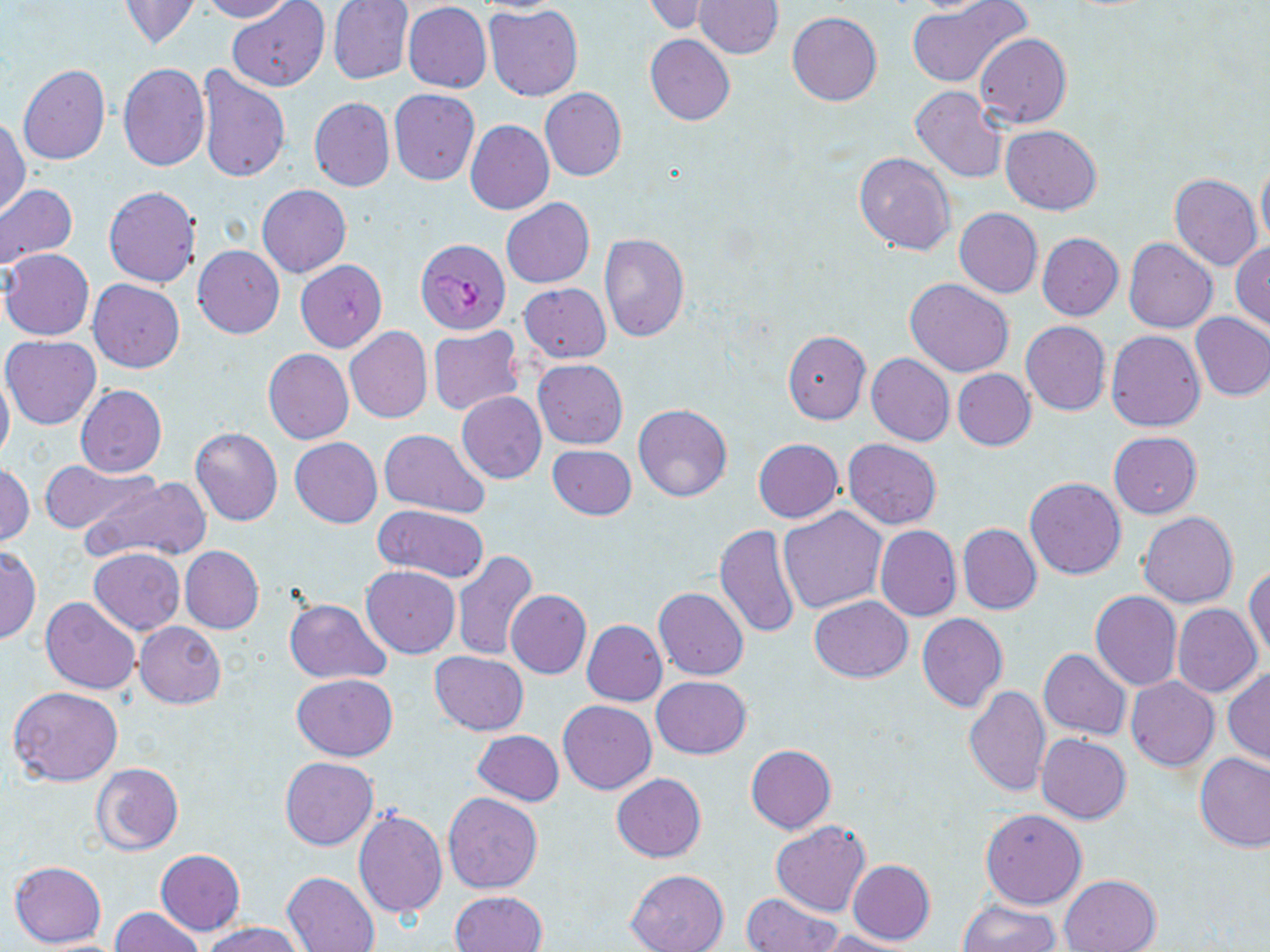
Approximate bounding boxes as named x1/y1/x2/y2 corners in pixels. Plasmodium falciparum-infected red blood cell locations: (x1=416, y1=238, x2=511, y2=334). Uninfected red blood cell locations: (x1=199, y1=0, x2=296, y2=22), (x1=641, y1=0, x2=720, y2=35), (x1=695, y1=0, x2=783, y2=58), (x1=903, y1=0, x2=1009, y2=16), (x1=119, y1=1, x2=201, y2=50), (x1=228, y1=1, x2=330, y2=91), (x1=327, y1=2, x2=414, y2=86), (x1=403, y1=2, x2=492, y2=93), (x1=907, y1=3, x2=1030, y2=88), (x1=484, y1=5, x2=583, y2=101), (x1=787, y1=11, x2=882, y2=105), (x1=975, y1=33, x2=1070, y2=127), (x1=645, y1=34, x2=735, y2=125), (x1=118, y1=63, x2=209, y2=172), (x1=18, y1=64, x2=110, y2=164), (x1=197, y1=64, x2=290, y2=183), (x1=910, y1=86, x2=1008, y2=183), (x1=541, y1=87, x2=626, y2=181), (x1=389, y1=89, x2=479, y2=186), (x1=310, y1=98, x2=395, y2=192), (x1=0, y1=117, x2=30, y2=217), (x1=877, y1=119, x2=985, y2=238), (x1=467, y1=121, x2=554, y2=215), (x1=1000, y1=125, x2=1102, y2=215), (x1=854, y1=151, x2=956, y2=256), (x1=1256, y1=162, x2=1270, y2=252), (x1=1169, y1=173, x2=1262, y2=271), (x1=0, y1=182, x2=77, y2=270), (x1=103, y1=185, x2=201, y2=287), (x1=257, y1=185, x2=351, y2=278), (x1=501, y1=198, x2=594, y2=288), (x1=954, y1=208, x2=1042, y2=297), (x1=598, y1=233, x2=689, y2=342), (x1=1036, y1=233, x2=1124, y2=321), (x1=1124, y1=238, x2=1217, y2=333), (x1=1230, y1=242, x2=1270, y2=332), (x1=193, y1=245, x2=284, y2=338), (x1=1, y1=249, x2=94, y2=341), (x1=295, y1=260, x2=388, y2=352), (x1=88, y1=278, x2=184, y2=373), (x1=905, y1=279, x2=1015, y2=377), (x1=520, y1=282, x2=611, y2=363), (x1=1190, y1=312, x2=1270, y2=402), (x1=1021, y1=320, x2=1110, y2=415), (x1=345, y1=326, x2=432, y2=423), (x1=428, y1=326, x2=523, y2=416), (x1=1105, y1=330, x2=1205, y2=431), (x1=782, y1=331, x2=871, y2=423), (x1=1, y1=335, x2=101, y2=429), (x1=263, y1=348, x2=353, y2=444), (x1=866, y1=353, x2=954, y2=447), (x1=534, y1=359, x2=628, y2=449), (x1=953, y1=369, x2=1035, y2=450), (x1=0, y1=370, x2=14, y2=466), (x1=76, y1=385, x2=167, y2=478), (x1=457, y1=392, x2=547, y2=483), (x1=633, y1=404, x2=733, y2=502), (x1=190, y1=427, x2=282, y2=526), (x1=379, y1=429, x2=490, y2=516), (x1=1109, y1=432, x2=1202, y2=518), (x1=291, y1=438, x2=381, y2=527), (x1=753, y1=439, x2=842, y2=523), (x1=843, y1=439, x2=941, y2=529), (x1=547, y1=444, x2=636, y2=520), (x1=42, y1=460, x2=156, y2=536), (x1=1, y1=464, x2=33, y2=547), (x1=81, y1=475, x2=212, y2=565), (x1=1025, y1=477, x2=1126, y2=579), (x1=373, y1=505, x2=488, y2=583), (x1=778, y1=507, x2=887, y2=614), (x1=1139, y1=511, x2=1238, y2=607), (x1=714, y1=523, x2=801, y2=639), (x1=957, y1=524, x2=1041, y2=615), (x1=875, y1=525, x2=962, y2=622), (x1=0, y1=546, x2=41, y2=643), (x1=180, y1=546, x2=264, y2=634), (x1=89, y1=548, x2=185, y2=634), (x1=451, y1=550, x2=539, y2=661), (x1=1246, y1=563, x2=1269, y2=663), (x1=361, y1=566, x2=460, y2=658), (x1=653, y1=586, x2=749, y2=681), (x1=505, y1=589, x2=591, y2=679), (x1=1090, y1=591, x2=1181, y2=690), (x1=809, y1=595, x2=913, y2=682), (x1=40, y1=597, x2=140, y2=695), (x1=283, y1=598, x2=391, y2=684), (x1=1173, y1=604, x2=1261, y2=697), (x1=917, y1=613, x2=1008, y2=712), (x1=581, y1=620, x2=666, y2=706), (x1=134, y1=621, x2=225, y2=708), (x1=1038, y1=649, x2=1131, y2=740), (x1=431, y1=652, x2=528, y2=735), (x1=1223, y1=668, x2=1270, y2=765), (x1=292, y1=675, x2=398, y2=760), (x1=651, y1=676, x2=751, y2=759), (x1=1125, y1=678, x2=1220, y2=772), (x1=9, y1=686, x2=124, y2=786), (x1=964, y1=686, x2=1051, y2=798), (x1=558, y1=700, x2=655, y2=794), (x1=472, y1=729, x2=564, y2=806), (x1=1037, y1=734, x2=1130, y2=823), (x1=745, y1=745, x2=836, y2=833), (x1=1194, y1=751, x2=1270, y2=851), (x1=280, y1=757, x2=378, y2=850), (x1=90, y1=763, x2=182, y2=855), (x1=612, y1=773, x2=706, y2=862), (x1=443, y1=792, x2=542, y2=894), (x1=353, y1=807, x2=448, y2=918), (x1=980, y1=809, x2=1087, y2=908), (x1=771, y1=820, x2=870, y2=917), (x1=155, y1=850, x2=246, y2=935), (x1=848, y1=859, x2=935, y2=944), (x1=9, y1=860, x2=108, y2=948), (x1=626, y1=868, x2=728, y2=952), (x1=283, y1=870, x2=380, y2=952), (x1=1059, y1=874, x2=1161, y2=952), (x1=451, y1=890, x2=548, y2=952), (x1=740, y1=894, x2=843, y2=952), (x1=959, y1=901, x2=1059, y2=952), (x1=109, y1=907, x2=204, y2=952), (x1=204, y1=921, x2=301, y2=952), (x1=820, y1=930, x2=917, y2=952). Slide-level diagnosis: Plasmodium falciparum. One field of a larger specimen. May-Grünwald-Giemsa stain. Optical microscopy. Thin blood smear. Captured at 1000x magnification. Image is 1270×952 pixels.